Assess this cell for malaria.
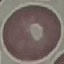
Uninfected.

capture = smartphone camera at the microscope eyepiece
preparation = thin smear
stain = Giemsa
image type = automatically extracted cell patch, resized to 64 × 64 pixels